Locate every WBC.
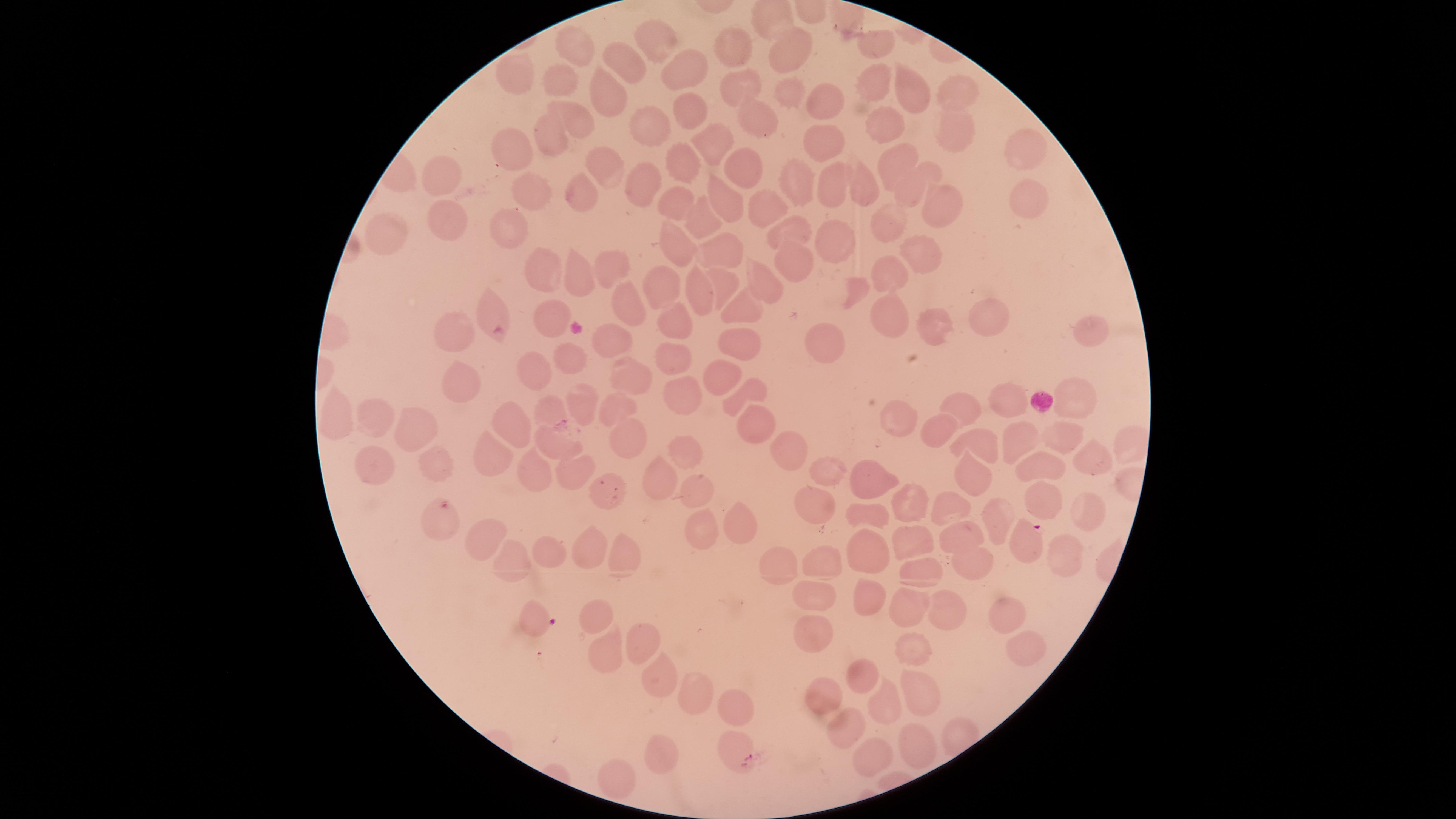
No WBCs identified.

Approximate marker points, in pixels from the top-left corner.
Summary:
  - Parasitized RBCs: (x=445, y=507), (x=1024, y=540), (x=536, y=618), (x=736, y=751)
  - Uninfected RBCs: (x=657, y=37), (x=879, y=40), (x=574, y=42), (x=738, y=46), (x=793, y=53), (x=619, y=60), (x=691, y=63), (x=519, y=79), (x=558, y=79), (x=870, y=81), (x=605, y=86), (x=956, y=88), (x=735, y=89), (x=914, y=89), (x=786, y=98), (x=815, y=104), (x=681, y=111), (x=749, y=117), (x=575, y=120), (x=880, y=121), (x=652, y=126), (x=951, y=127), (x=550, y=131), (x=710, y=139), (x=814, y=139), (x=1021, y=147), (x=517, y=151), (x=894, y=158), (x=687, y=162), (x=743, y=165), (x=606, y=171), (x=442, y=174), (x=867, y=177), (x=646, y=180), (x=796, y=183), (x=836, y=185), (x=904, y=185), (x=532, y=193), (x=575, y=194), (x=1017, y=197), (x=730, y=198), (x=770, y=200), (x=935, y=200), (x=672, y=203), (x=893, y=219), (x=446, y=220), (x=698, y=220), (x=514, y=228), (x=794, y=228), (x=387, y=231), (x=830, y=242), (x=681, y=244), (x=726, y=252), (x=915, y=254), (x=796, y=263), (x=607, y=268), (x=544, y=270), (x=579, y=270), (x=893, y=271), (x=767, y=282), (x=725, y=283), (x=663, y=289), (x=701, y=289), (x=857, y=292), (x=629, y=298), (x=747, y=309), (x=490, y=310), (x=551, y=317), (x=890, y=319), (x=677, y=320), (x=981, y=323), (x=928, y=327), (x=451, y=333), (x=1092, y=333), (x=742, y=340), (x=614, y=342), (x=831, y=342), (x=573, y=353), (x=675, y=356), (x=528, y=368), (x=627, y=370), (x=727, y=372), (x=459, y=381), (x=681, y=397), (x=1074, y=397), (x=741, y=398), (x=583, y=401), (x=1012, y=401), (x=968, y=407), (x=618, y=409), (x=898, y=409), (x=554, y=410), (x=751, y=414), (x=340, y=419), (x=375, y=421), (x=937, y=424), (x=509, y=425), (x=414, y=426), (x=1062, y=433), (x=550, y=440), (x=630, y=441), (x=1017, y=442), (x=984, y=443), (x=796, y=448), (x=493, y=449), (x=691, y=453), (x=1088, y=461), (x=376, y=464), (x=438, y=466), (x=1033, y=470), (x=531, y=471), (x=826, y=472), (x=972, y=477), (x=569, y=478), (x=876, y=479), (x=656, y=481), (x=693, y=491), (x=606, y=494), (x=1037, y=495), (x=819, y=498), (x=909, y=499), (x=953, y=504), (x=1075, y=509), (x=869, y=510), (x=991, y=516), (x=731, y=520), (x=484, y=532), (x=696, y=532), (x=914, y=540), (x=960, y=541), (x=863, y=548), (x=545, y=549), (x=585, y=550), (x=1052, y=553), (x=622, y=554), (x=504, y=557), (x=779, y=561), (x=822, y=561), (x=969, y=567), (x=917, y=569), (x=815, y=597), (x=873, y=598), (x=909, y=608), (x=940, y=608), (x=1006, y=612), (x=602, y=615), (x=809, y=634), (x=640, y=644), (x=1018, y=646), (x=604, y=654), (x=906, y=654), (x=658, y=670), (x=859, y=677), (x=916, y=685), (x=692, y=695), (x=822, y=697), (x=733, y=704), (x=884, y=708), (x=847, y=724), (x=918, y=739), (x=659, y=749), (x=876, y=754), (x=620, y=777)
  - Preparation: thin blood film
  - Species: Plasmodium falciparum
  - Field of view: single
  - Visible region: circular
  - Stain: Giemsa
  - Image size: 1456×819 pixels
  - Presence: malaria parasites detected
  - Capture: smartphone photograph through the microscope eyepiece